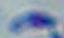

identification = Toxoplasma gondii
magnification = 1000x
modality = photomicrograph